Name the parasite shown.
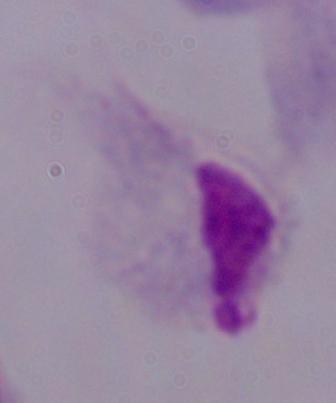

This is a trichomonad.

Photomicrograph. Captured at 1000x magnification.